Comment on the morphology of the red blood cells.
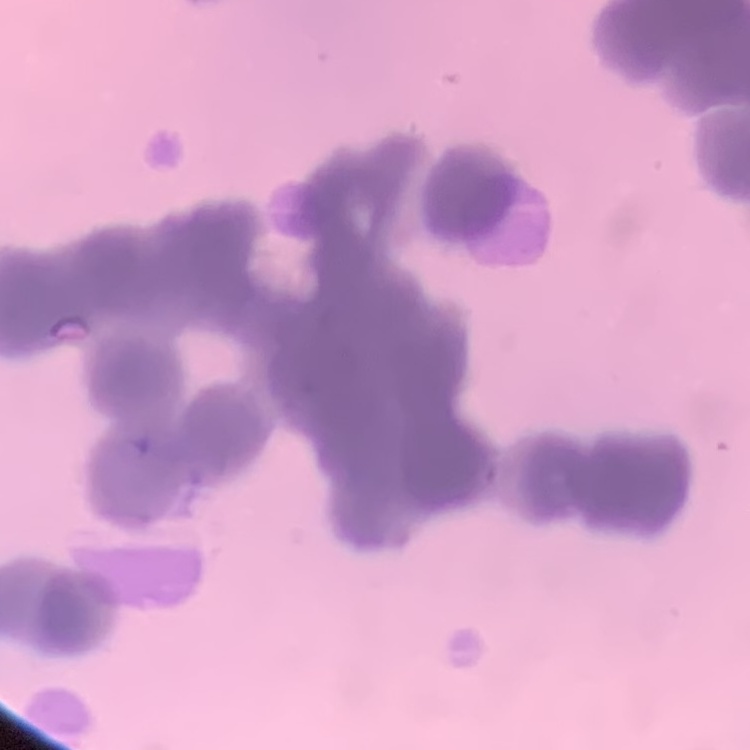
Rouleaux formation.

Summary:
  - Preparation: thin blood film
  - Image type: one tile cut from a larger photomicrograph
  - Stain: Field's or Giemsa